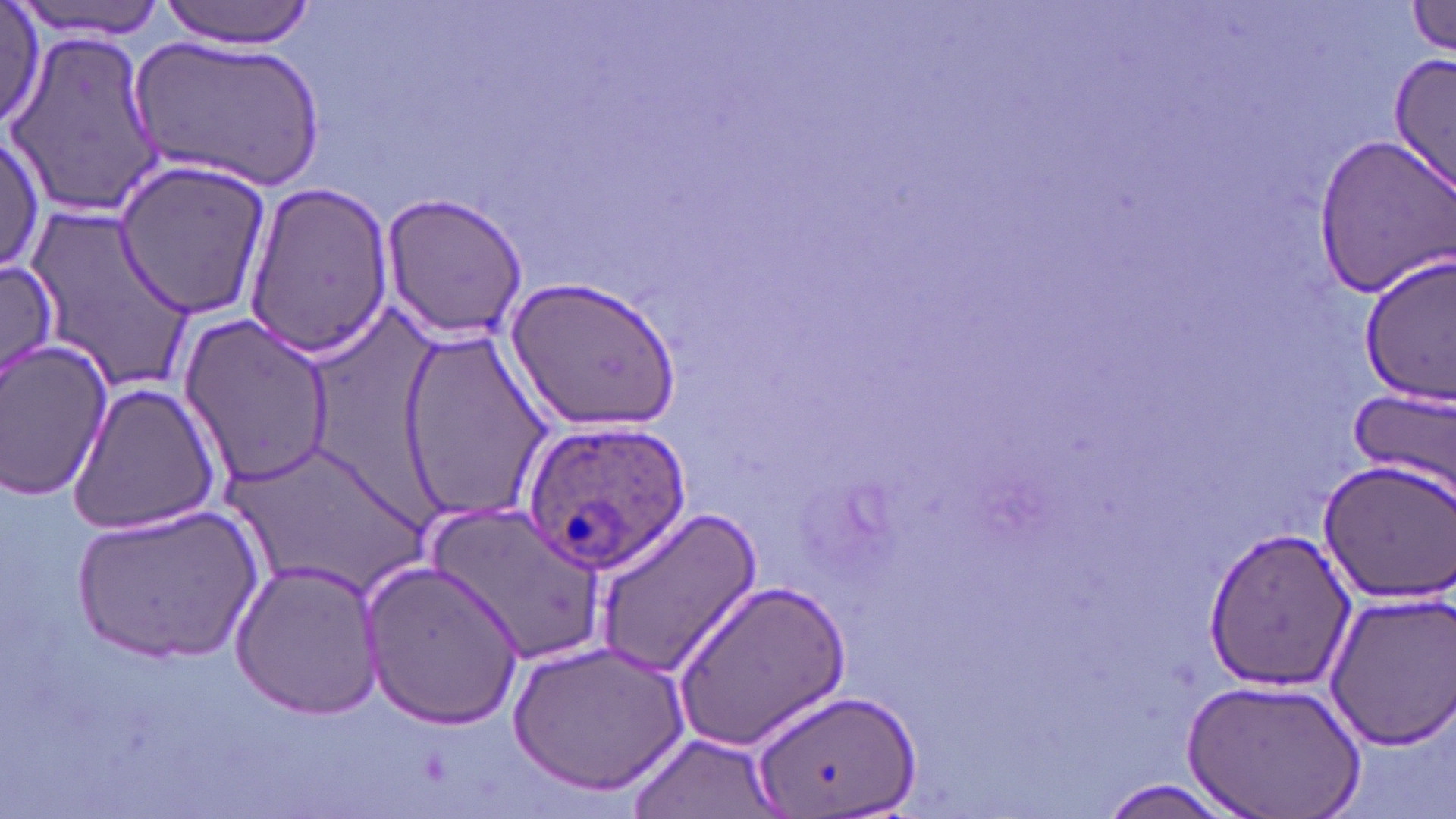
Summary:
  - Coordinate format: approximate bounding boxes as [x1, y1, x2, y2] in pixels
  - Uninfected red blood cell locations: [12, 0, 169, 39], [158, 0, 316, 47], [1405, 0, 1456, 57], [0, 1, 46, 136], [4, 29, 163, 217], [130, 31, 329, 191], [1388, 54, 1456, 199], [1313, 131, 1456, 297], [0, 134, 46, 274], [111, 157, 276, 317], [243, 179, 396, 361], [379, 191, 529, 341], [25, 203, 198, 396], [1359, 254, 1456, 406], [0, 261, 65, 382], [507, 273, 682, 430], [176, 308, 337, 489], [396, 328, 552, 521], [0, 337, 115, 502], [69, 381, 222, 538], [1347, 386, 1456, 502], [217, 439, 435, 599], [1317, 459, 1456, 605], [74, 501, 256, 666], [428, 504, 604, 663], [595, 509, 762, 678], [1202, 528, 1356, 692], [361, 557, 525, 732], [229, 559, 383, 718], [672, 577, 851, 750], [1319, 590, 1455, 749], [509, 638, 688, 796], [1187, 677, 1365, 819], [752, 684, 919, 818], [627, 733, 778, 816], [1095, 778, 1250, 819]
  - Plasmodium ovale-infected red blood cell locations: [517, 417, 692, 575]
  - Slide-level diagnosis: Plasmodium ovale
  - Modality: optical microscopy
  - Magnification: 1000x
  - Stain: May-Grünwald-Giemsa
  - Preparation: thin blood film
  - Field of view: single
  - Image size: 1456×819 pixels